Report the malaria status of this cell.
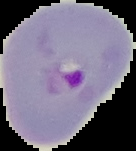
It is parasitized.

Image is 136×151 pixels. Segmented cell region on a black background. From a thin blood smear.